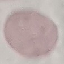

malaria status = uninfected
preparation = thin blood film
stain = Giemsa
capture = smartphone through the microscope eyepiece
image type = cell patch, automatically extracted from a larger field of view and resized to 64 × 64 pixels